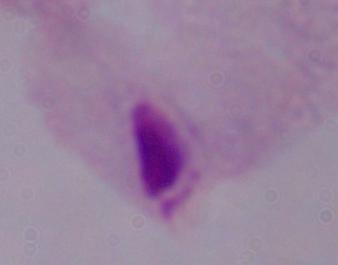 A trichomonad is shown. Captured at 1000x magnification. Micrograph.